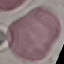
Summary:
  - Malaria status: uninfected
  - Image type: automatically extracted cell patch, resized to 64 × 64 pixels
  - Capture: smartphone camera at the microscope eyepiece
  - Stain: Giemsa
  - Preparation: thin blood smear